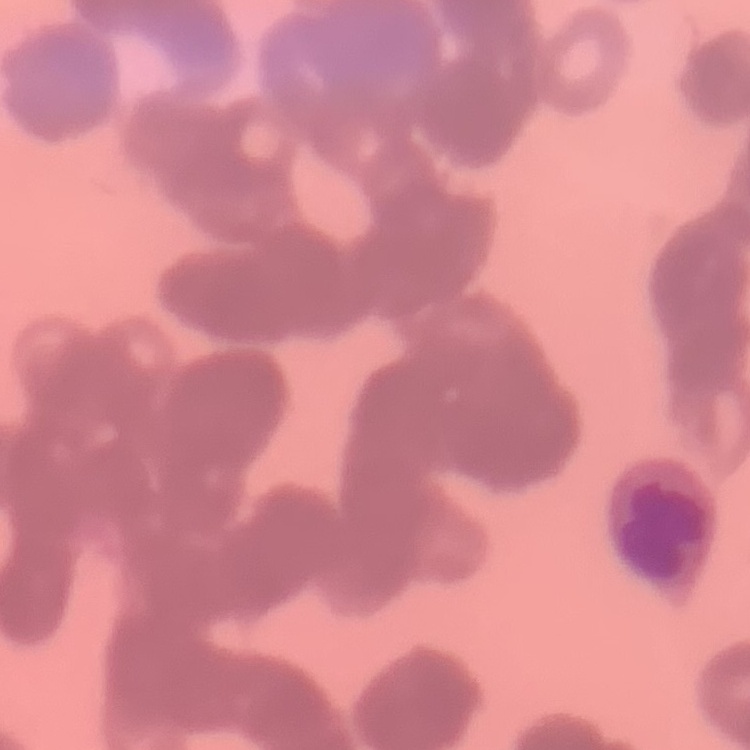
The erythrocytes show rouleaux formation. One tile cut from a larger photomicrograph. Thin peripheral smear. Field's or Giemsa stain.